Classify this cell by malaria status.
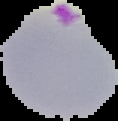
It is parasitized.

image size = 118×121 pixels
preparation = thin blood smear
image type = segmented cell region on a black background